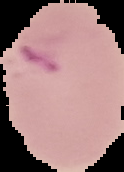

{
  "image_size": "124×172 pixels",
  "preparation": "thin blood film",
  "image_type": "segmented cell region with the area outside set to black",
  "malaria_status": "parasitized"
}